Classify this cell by malaria status.
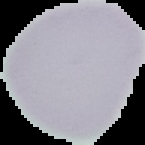
Uninfected.

{
  "preparation": "thin blood film",
  "image_size": "145×145 pixels",
  "image_type": "cell region segmented out of the field of view; surrounding area masked to black"
}